Name the parasite shown.
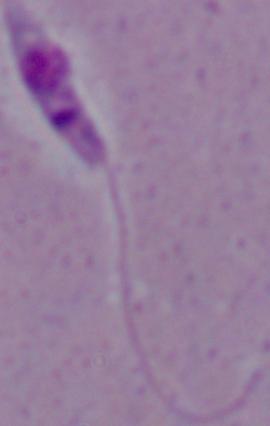

Leishmania.

Photomicrograph. Captured at 1000x magnification.